Assess the morphology of the red blood cells.
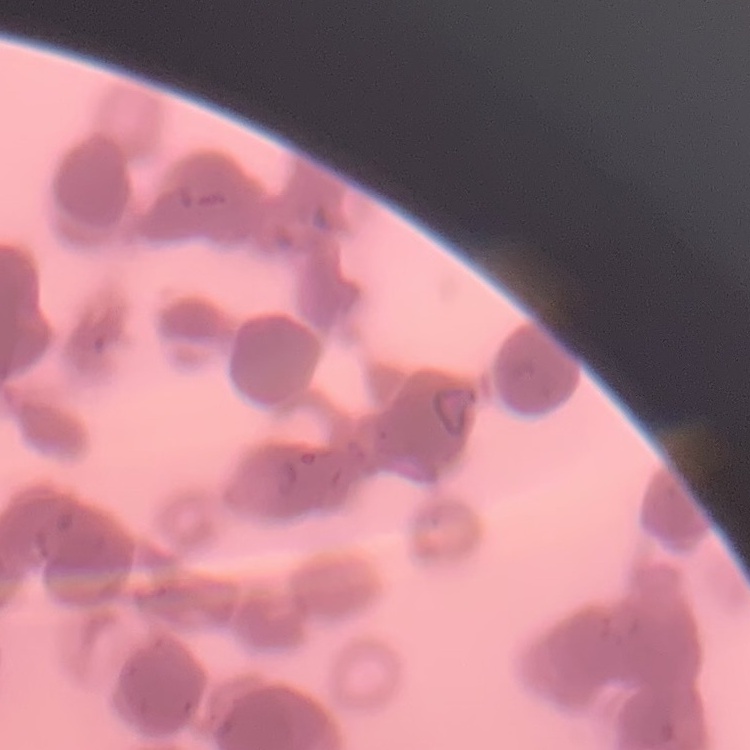
Rouleaux formation.

stain: Field's or Giemsa
image_type: square crop of a larger photomicrograph
preparation: thin blood film